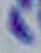

Summary:
  - Identification: Toxoplasma gondii
  - Modality: photomicrograph
  - Magnification: 1000x